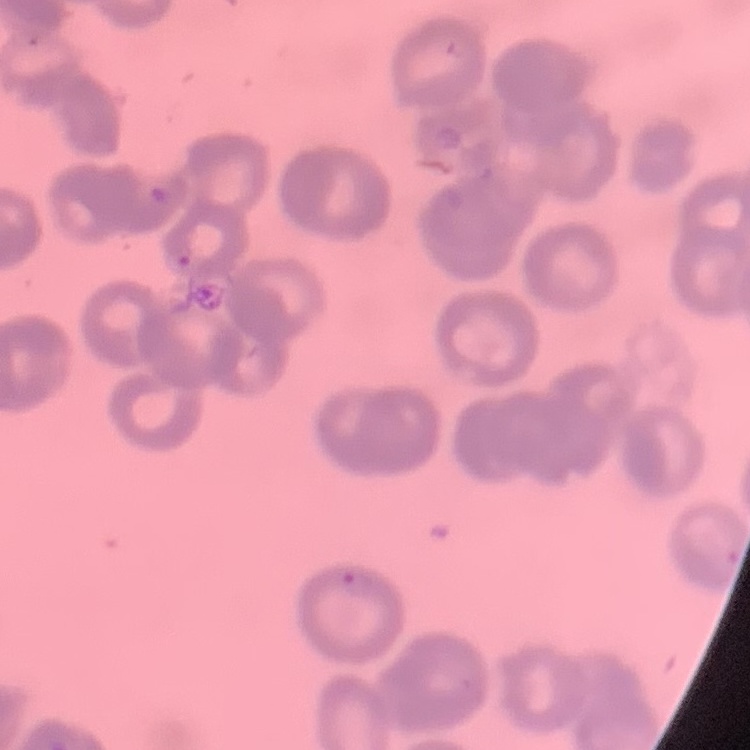

Summary:
  - Erythrocyte morphology: rouleaux formation
  - Preparation: thin blood smear
  - Stain: Field's or Giemsa
  - Image type: one tile cut from a larger photomicrograph